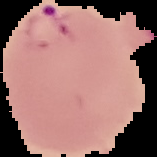
Summary:
  - Image type: segmented cell region on a black background
  - Result: Plasmodium parasites detected
  - Image size: 157×157 pixels
  - Preparation: thin blood smear